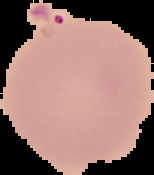
{
  "image_type": "segmented cell region with the area outside set to black",
  "image_size": "154×175 pixels",
  "result": "no malaria parasites detected",
  "preparation": "thin blood smear"
}